Locate every blood parasite and identify its species.
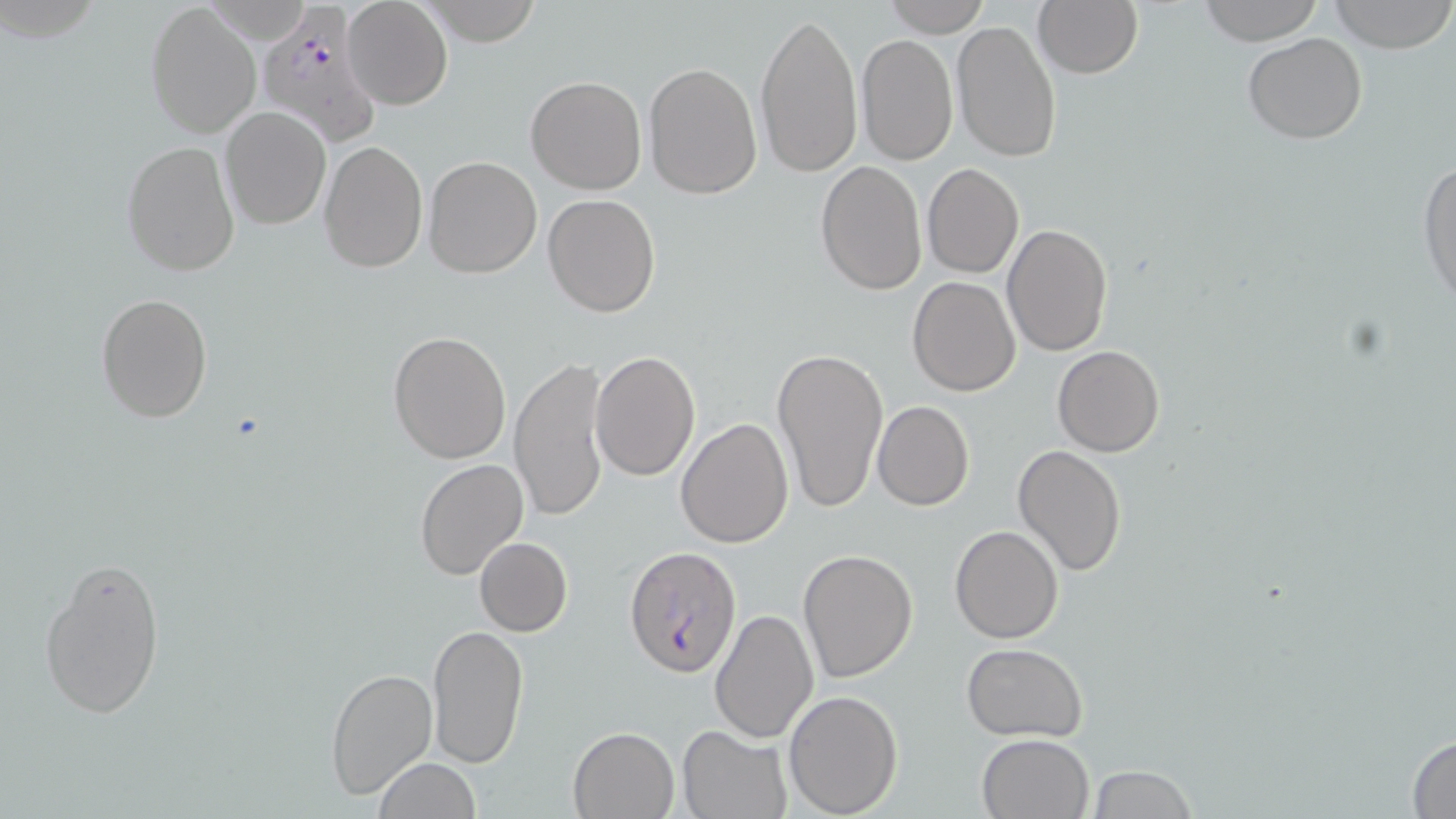

Approximate bounding boxes as (x1,y1)-(x2,y2) corner pairs in pixels.
Plasmodium falciparum-infected red blood cells: (256,9)-(379,145), (622,546)-(741,678).
No Plasmodium ovale, Plasmodium malariae, Plasmodium vivax, Babesia divergens, or Trypanosoma brucei observed.

Summary:
  - Uninfected red blood cell locations: (342,0)-(452,110), (420,0)-(545,46), (882,0)-(992,38), (1033,0)-(1142,80), (1197,0)-(1324,45), (1330,0)-(1455,52), (145,1)-(262,140), (754,8)-(864,180), (952,20)-(1061,161), (1241,32)-(1369,145), (856,34)-(959,166), (643,62)-(763,199), (525,75)-(646,195), (220,106)-(331,230), (317,140)-(427,272), (122,141)-(241,277), (422,155)-(542,278), (1417,157)-(1456,310), (814,159)-(927,296), (921,163)-(1023,279), (542,193)-(662,318), (1003,222)-(1114,359), (906,276)-(1021,396), (95,294)-(212,423), (387,331)-(512,465), (1052,345)-(1165,457), (771,346)-(888,515), (590,350)-(701,481), (509,356)-(611,524), (873,400)-(974,511), (676,418)-(794,549), (1012,445)-(1126,577), (415,456)-(528,580), (949,525)-(1064,643), (473,537)-(572,637), (797,549)-(920,685), (38,553)-(165,721), (709,608)-(819,744), (427,623)-(530,769), (961,642)-(1088,741), (324,667)-(438,800), (784,689)-(903,815), (677,724)-(793,818), (569,726)-(680,818), (977,732)-(1094,818), (1405,732)-(1455,817), (372,758)-(483,818), (1085,765)-(1198,819)
  - Slide-level diagnosis: Plasmodium falciparum
  - Field of view: single
  - Preparation: thin blood film
  - Stain: May-Grünwald-Giemsa
  - Magnification: 1000x
  - Modality: light microscopy
  - Image size: 1456×819 pixels